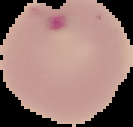

image type = cell region segmented out of the field of view; surrounding area masked to black
image size = 133×127 pixels
preparation = thin blood smear
result = Plasmodium parasites detected